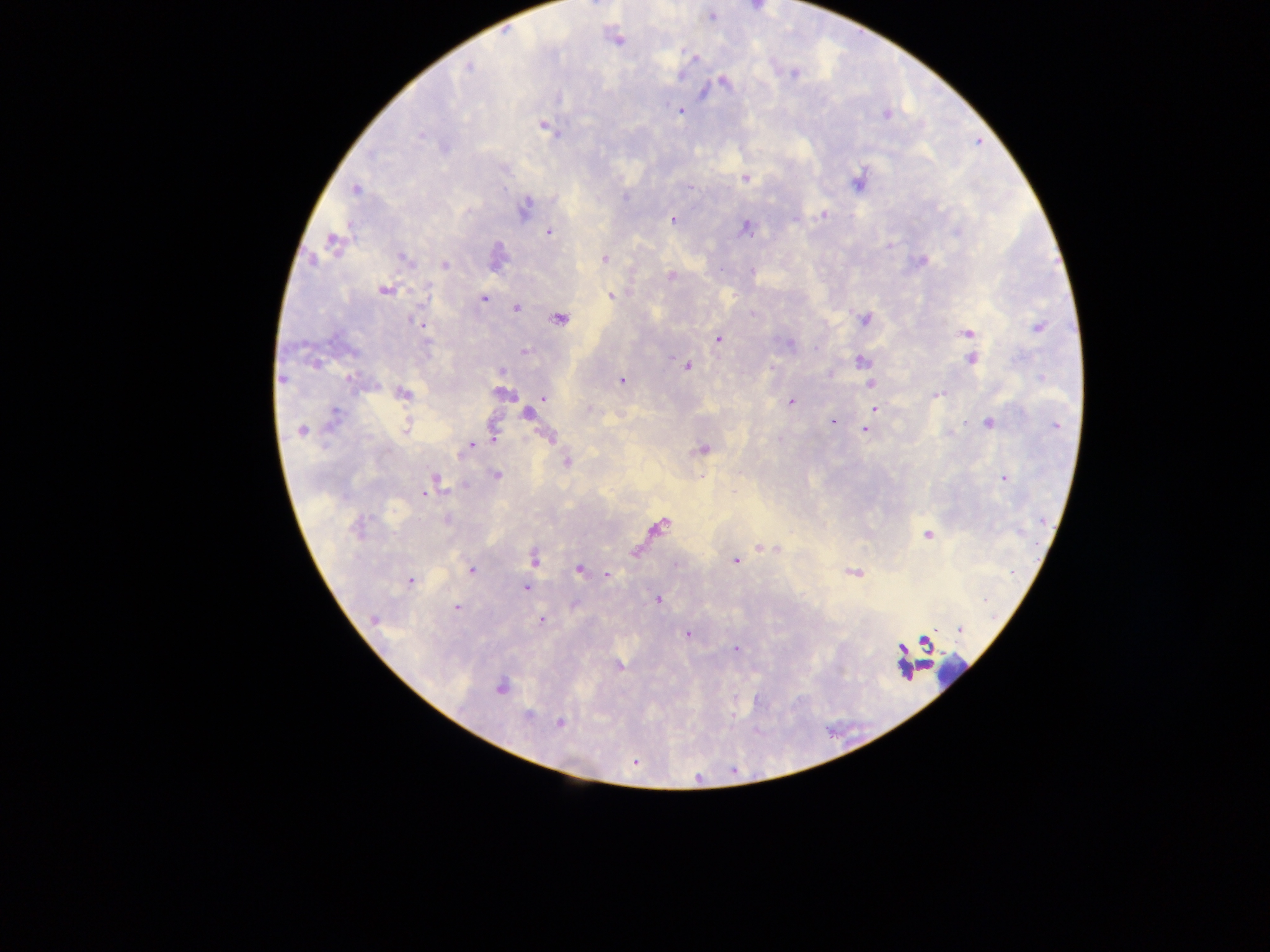

leukocyte_locations: 'approximate centers as x y in pixels: 913 658; 953 672'
field_of_view: single
preparation: thick blood film
image_size: 1270×952 pixels
country: Ghana
capture: mobile-phone photograph through a microscope
malaria_parasite_locations: 'approximate centers as x y in pixels: 615 39; 693 58; 469 67; 722 81; 681 110; 886 113; 544 125; 745 178; 858 183; 356 189; 522 206; 823 215; 673 220; 745 227; 548 232; 332 241; 495 256; 605 258; 405 260; 920 261; 445 265; 670 275; 384 289; 610 295; 482 298; 516 308; 559 318; 864 318; 1039 327; 967 333; 718 338; 524 352; 971 358; 860 360; 316 363; 686 366; 772 368; 281 377; 621 380; 867 380; 871 383; 403 393; 502 394; 936 394; 543 398; 791 401; 588 409; 875 409; 526 413; 831 421; 988 422; 1055 425; 406 427; 864 429; 302 431; 492 432; 548 437; 470 445; 702 449; 566 461; 495 475; 1004 478; 436 479; 424 494; 448 519; 659 526; 927 534; 761 547; 772 548; 534 558; 736 560; 471 569; 578 569; 853 572; 606 576; 409 580; 526 587; 656 598; 574 606; 456 607; 374 619; 541 620; 959 629; 686 634; 735 648; 618 665; 500 686; 559 723; 634 761'